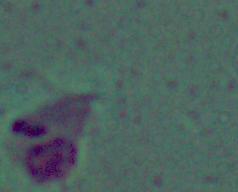
identification = Leishmania
magnification = 1000x
modality = photomicrograph